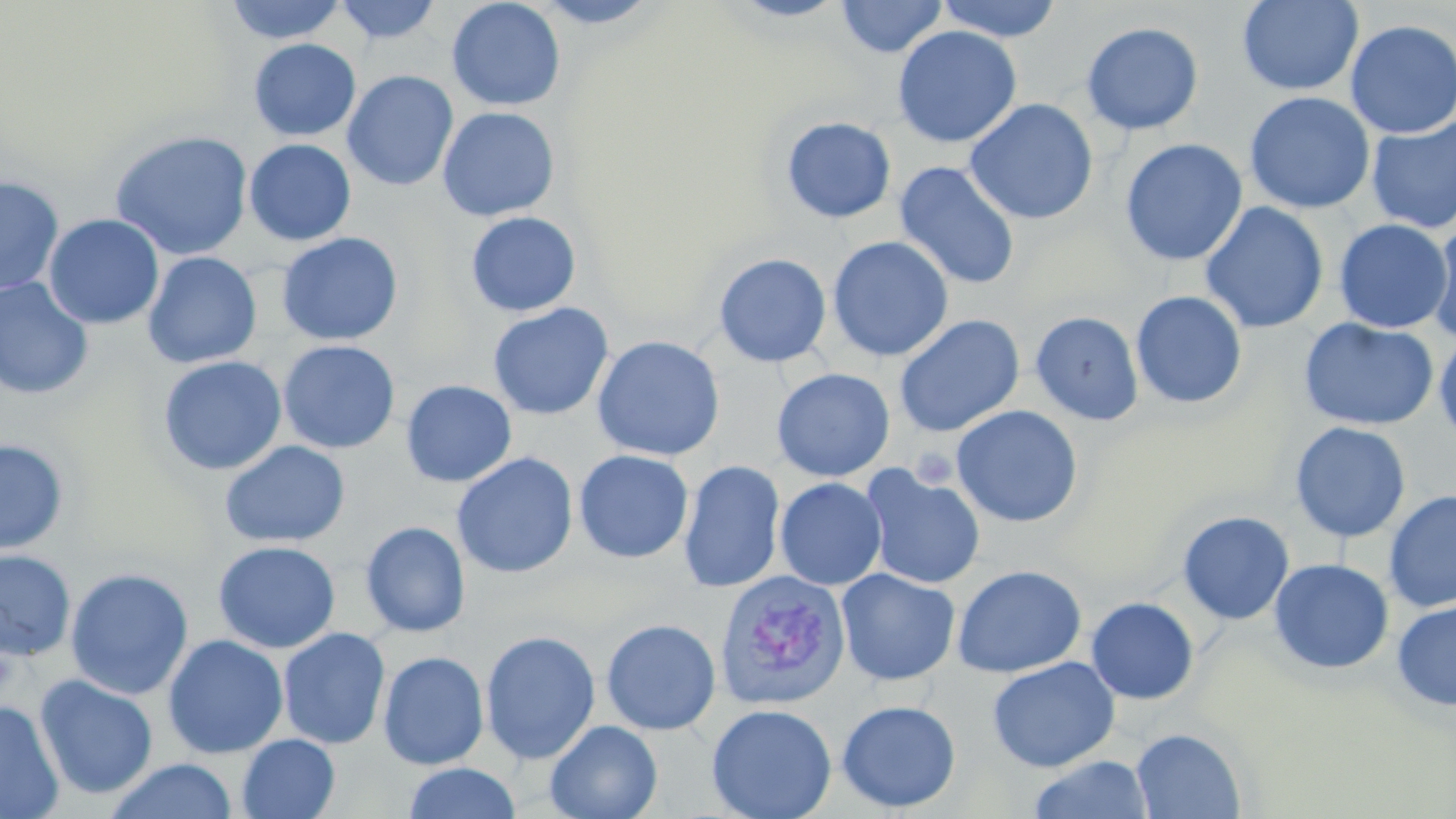
Approximate bounding boxes as (x1, y1, x2, y2) in pixels. Platelet locations: (911, 447, 958, 488). Plasmodium vivax-infected red blood cell locations: (715, 569, 850, 710). Uninfected red blood cell locations: (224, 0, 348, 44), (334, 0, 442, 45), (446, 0, 566, 112), (528, 0, 666, 28), (723, 0, 854, 23), (835, 0, 948, 58), (935, 0, 1064, 42), (1237, 0, 1364, 96), (843, 2, 985, 90), (1344, 19, 1456, 139), (1081, 22, 1204, 135), (892, 25, 1022, 148), (248, 38, 361, 141), (342, 70, 459, 191), (1244, 92, 1375, 214), (964, 98, 1099, 226), (437, 106, 560, 222), (780, 116, 897, 223), (1366, 117, 1456, 233), (109, 130, 253, 261), (244, 138, 356, 246), (1120, 138, 1247, 267), (894, 161, 1021, 290), (0, 174, 63, 297), (1200, 201, 1329, 334), (465, 211, 581, 317), (43, 213, 164, 329), (1333, 219, 1454, 334), (1428, 220, 1456, 348), (276, 232, 404, 346), (827, 235, 954, 362), (142, 251, 262, 369), (713, 253, 832, 368), (0, 278, 94, 399), (1130, 290, 1247, 410), (487, 302, 614, 421), (1030, 311, 1144, 426), (893, 314, 1025, 437), (1298, 317, 1439, 431), (1433, 332, 1456, 446), (591, 335, 725, 462), (278, 339, 401, 454), (158, 355, 287, 476), (772, 368, 895, 482), (401, 379, 517, 488), (951, 405, 1084, 528), (1289, 421, 1411, 543), (0, 438, 69, 554), (219, 440, 351, 548), (573, 449, 694, 563), (452, 453, 578, 579), (678, 459, 786, 592), (862, 466, 985, 590), (775, 477, 886, 590), (1383, 490, 1456, 613), (1177, 510, 1294, 625), (360, 521, 470, 637), (212, 540, 340, 654), (0, 549, 76, 661), (1268, 558, 1394, 675), (951, 564, 1087, 678), (65, 568, 194, 700), (836, 568, 960, 686), (1085, 597, 1199, 705), (1392, 600, 1456, 712), (601, 618, 721, 735), (277, 627, 390, 749), (480, 630, 600, 764), (162, 634, 288, 759), (378, 650, 488, 770), (986, 656, 1121, 773), (34, 675, 158, 800), (0, 699, 64, 819), (836, 699, 961, 812), (706, 703, 837, 819), (545, 719, 663, 819), (1131, 728, 1247, 818), (237, 734, 340, 819), (1029, 754, 1153, 818), (105, 759, 239, 819), (402, 763, 522, 819). Slide-level diagnosis: Plasmodium vivax. One field of a larger specimen. Thin blood smear. May-Grünwald-Giemsa-stained preparation. Optical microscopy. Captured at 1000x magnification. Image is 1456×819 pixels.